Locate every uninfected red blood cell.
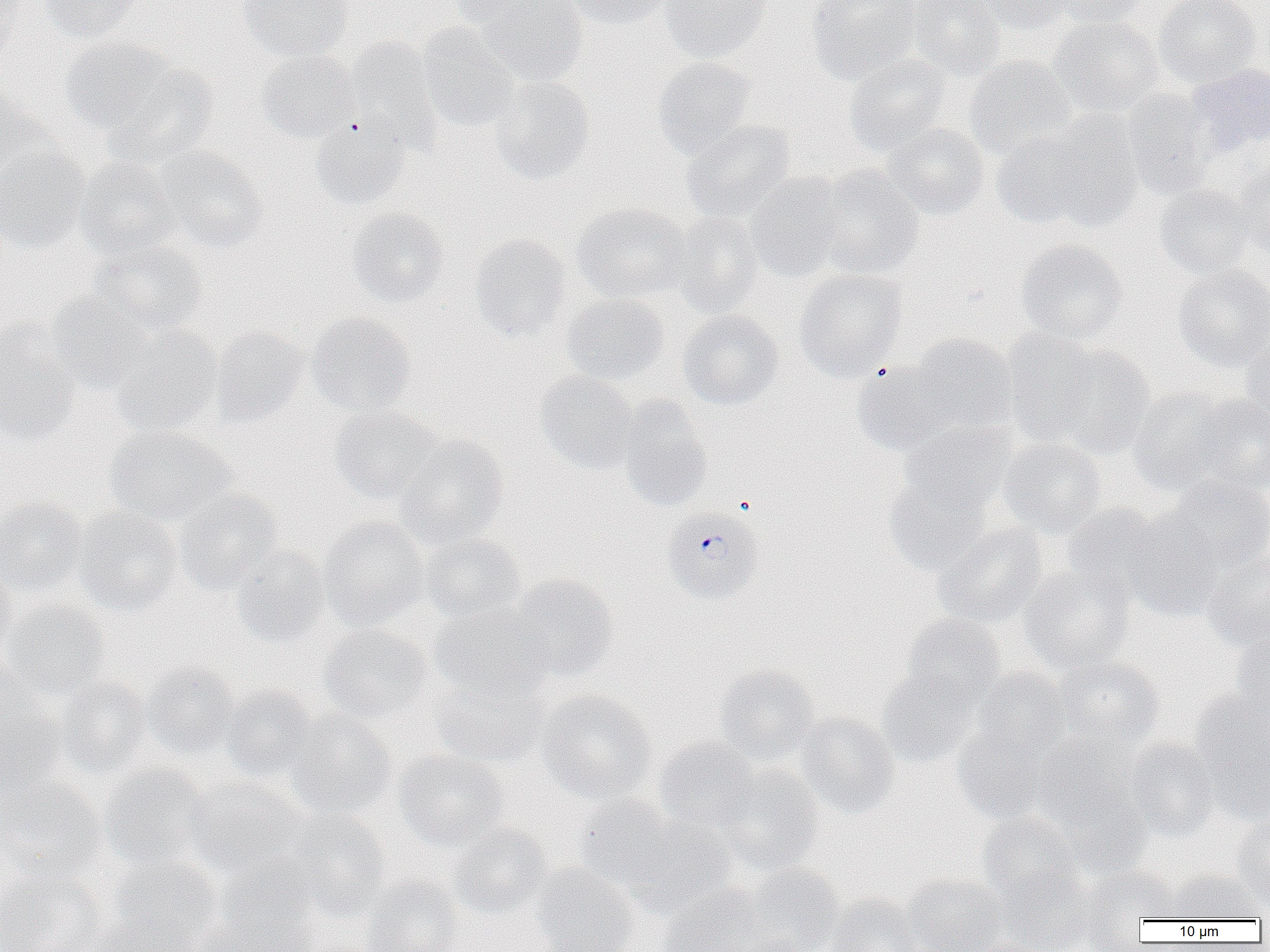
Approximate bounding boxes as (x1,y1)-(x2,y2) corner pairs in pixels.
Uninfected red blood cells: (0,0)-(27,66), (36,0)-(145,43), (237,0)-(354,63), (447,0)-(551,29), (479,0)-(588,85), (564,0)-(674,30), (659,0)-(772,62), (806,0)-(921,84), (906,0)-(1006,80), (974,0)-(1074,34), (1048,0)-(1147,28), (1154,0)-(1260,87), (1048,16)-(1165,117), (417,23)-(520,133), (59,37)-(177,135), (346,37)-(442,151), (256,51)-(359,143), (843,54)-(952,157), (964,55)-(1076,160), (652,56)-(755,158), (105,61)-(220,166), (1188,62)-(1270,155), (490,75)-(595,184), (0,87)-(51,188), (1121,89)-(1216,198), (1015,112)-(1146,233), (310,117)-(411,210), (681,119)-(795,223), (884,122)-(990,219), (0,143)-(90,252), (155,147)-(268,253), (74,158)-(182,262), (1231,162)-(1270,258), (812,166)-(925,279), (744,173)-(849,282), (1154,184)-(1259,278), (572,202)-(690,303), (346,206)-(449,308), (667,212)-(763,317), (470,233)-(572,343), (1015,239)-(1129,344), (90,240)-(206,338), (1172,264)-(1270,371), (794,268)-(908,381), (46,290)-(155,394), (560,293)-(671,386), (677,310)-(784,409), (306,312)-(416,417), (0,325)-(82,444), (109,326)-(223,437), (210,328)-(309,426), (1001,329)-(1105,445), (905,334)-(1018,436), (1239,337)-(1270,436), (1045,344)-(1156,457), (851,361)-(958,457), (535,371)-(637,473), (1126,386)-(1238,496), (1190,394)-(1270,496), (617,396)-(714,511), (329,406)-(441,503), (900,419)-(1016,512), (104,425)-(235,527), (394,433)-(508,548), (998,437)-(1106,538), (884,475)-(993,577), (1162,476)-(1270,575), (175,489)-(284,595), (0,497)-(89,597), (1062,503)-(1171,607), (72,508)-(183,616), (1121,511)-(1225,622), (319,516)-(429,631), (932,523)-(1048,628), (419,532)-(526,624), (231,545)-(331,649), (1201,551)-(1270,652), (0,561)-(17,664), (1019,565)-(1135,675), (507,574)-(619,682), (1,599)-(110,701), (428,604)-(551,701), (902,614)-(1006,707), (319,625)-(435,724), (1232,626)-(1270,734), (1049,656)-(1164,750), (142,661)-(239,759), (713,663)-(821,766), (877,666)-(982,768), (972,668)-(1071,761), (430,672)-(549,768), (0,674)-(66,798), (55,675)-(153,779), (220,685)-(320,783), (536,689)-(657,803), (1189,690)-(1270,824), (286,710)-(398,818), (795,712)-(899,818), (952,717)-(1058,823), (1031,733)-(1139,829), (654,738)-(761,831), (1124,739)-(1220,840), (394,749)-(509,851), (99,763)-(209,871), (712,766)-(823,875), (0,777)-(108,883), (184,778)-(306,881), (1053,786)-(1153,878), (575,795)-(682,895), (281,809)-(391,918), (1232,811)-(1270,908), (978,812)-(1081,903), (627,814)-(736,916), (447,822)-(555,920), (108,855)-(222,950), (202,863)-(322,952), (530,863)-(640,952), (741,864)-(845,952), (997,866)-(1096,952), (1078,867)-(1181,938), (0,868)-(106,952), (1166,870)-(1265,921), (903,874)-(1008,952), (359,875)-(464,952), (658,882)-(770,952), (824,893)-(923,952), (84,915)-(194,952), (963,938)-(1052,952).

Plasmodium falciparum-infected red blood cell locations: (662,506)-(764,605). Slide-level diagnosis: Plasmodium falciparum. One field of a larger specimen. Light microscopy. Image is 1270×952 pixels. Thin blood smear. 1000x magnification.